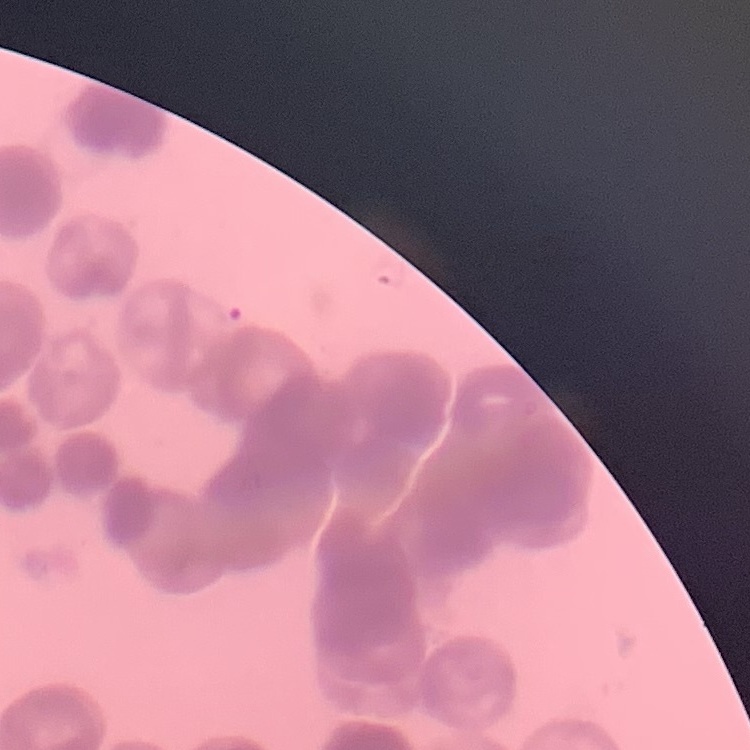
erythrocyte_morphology: rouleaux formation
image_type: square crop of a larger photomicrograph
preparation: thin peripheral smear
stain: Field's or Giemsa